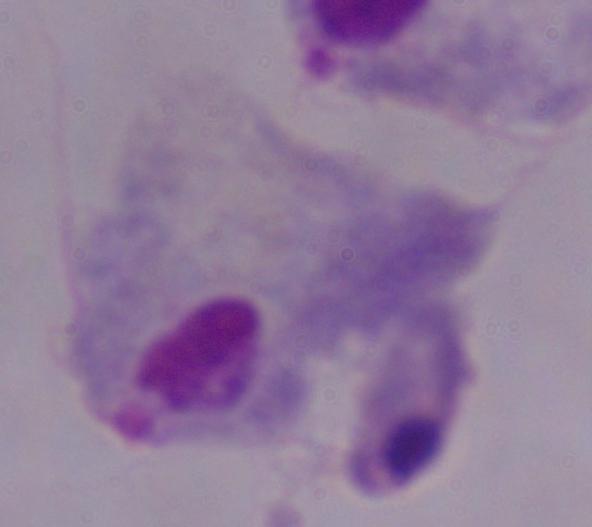
magnification = 1000x
identification = trichomonad
modality = photomicrograph